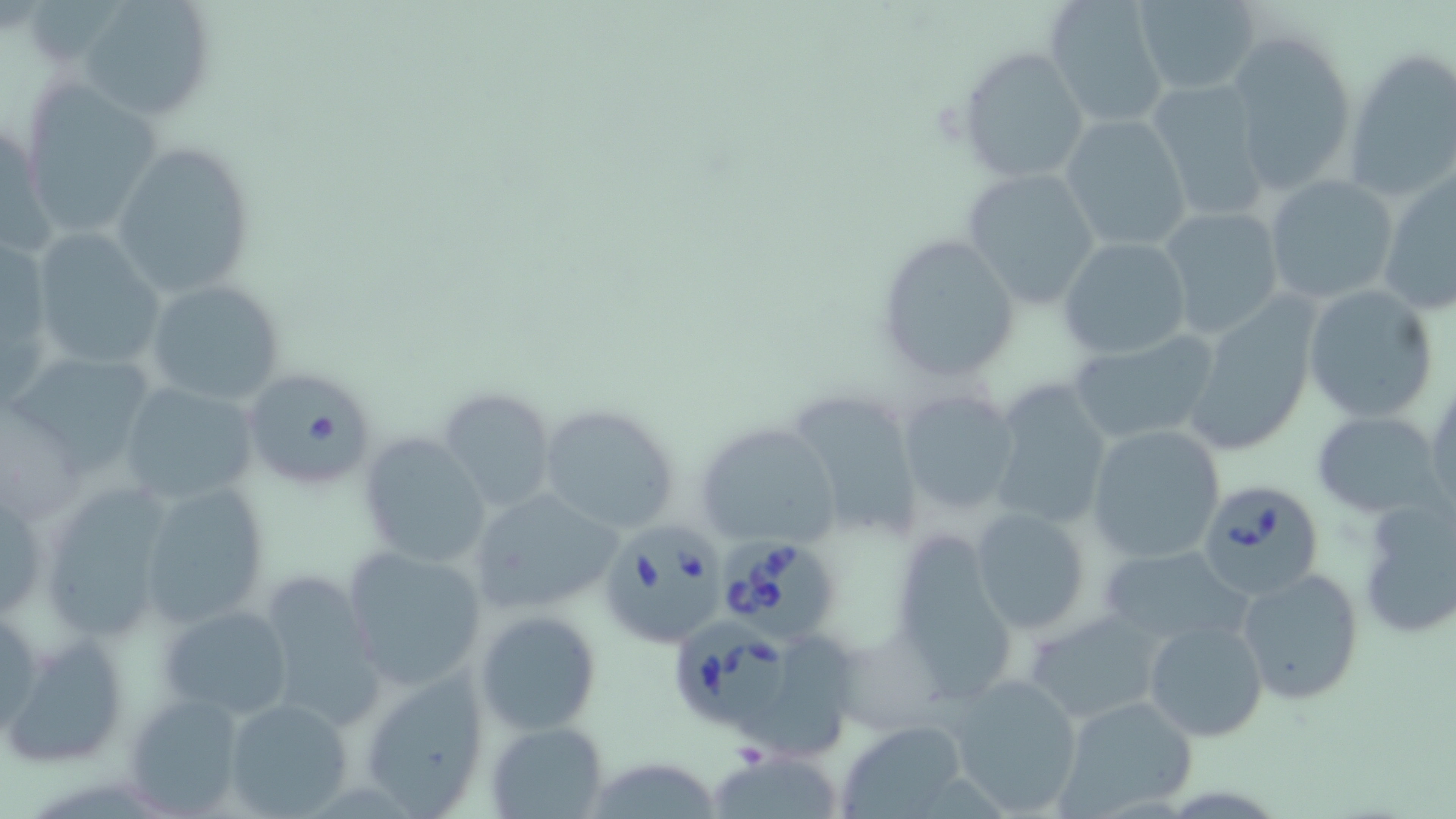

Summary:
  - Coordinate format: approximate bounding boxes as [x1, y1, x2, y2] in pixels
  - Uninfected red blood cell locations: [72, 0, 219, 121], [1045, 0, 1171, 129], [1130, 0, 1262, 95], [1226, 30, 1357, 197], [1341, 46, 1455, 201], [956, 47, 1090, 184], [1146, 78, 1271, 223], [21, 80, 165, 243], [1059, 114, 1194, 253], [112, 140, 257, 295], [1377, 163, 1456, 317], [960, 167, 1102, 310], [1264, 174, 1400, 306], [1158, 207, 1285, 339], [30, 230, 166, 377], [1, 233, 55, 409], [873, 233, 1023, 383], [1056, 235, 1193, 359], [144, 280, 286, 405], [1303, 285, 1438, 421], [1182, 297, 1323, 456], [1068, 332, 1221, 448], [12, 342, 159, 475], [240, 366, 378, 489], [1426, 372, 1455, 521], [986, 379, 1115, 531], [118, 383, 263, 502], [784, 383, 924, 546], [437, 386, 557, 514], [895, 388, 1021, 517], [535, 404, 681, 535], [1312, 410, 1444, 517], [695, 420, 844, 550], [1086, 424, 1225, 564], [358, 433, 491, 569], [46, 475, 181, 646], [135, 480, 274, 629], [467, 488, 623, 613], [1354, 494, 1456, 637], [969, 505, 1093, 635], [885, 531, 1023, 699], [1095, 544, 1253, 650], [342, 546, 489, 689], [1235, 567, 1365, 703], [255, 572, 384, 735], [157, 602, 296, 722], [474, 611, 603, 738], [1024, 612, 1170, 723], [1142, 617, 1269, 743], [5, 632, 129, 768], [748, 632, 858, 759], [356, 669, 490, 815], [944, 671, 1084, 816], [123, 690, 249, 814], [1054, 695, 1200, 817], [221, 696, 356, 817], [835, 719, 972, 817], [487, 721, 609, 818], [707, 745, 848, 819]
  - Babesia divergens-infected red blood cell locations: [1194, 479, 1325, 602], [602, 518, 740, 648], [718, 533, 843, 647], [674, 614, 803, 732]
  - Slide-level diagnosis: Babesia divergens
  - Modality: light microscopy
  - Image size: 1456×819 pixels
  - Magnification: 1000x
  - Stain: May-Grünwald-Giemsa
  - Preparation: thin blood smear
  - Field of view: single